Name the parasite shown.
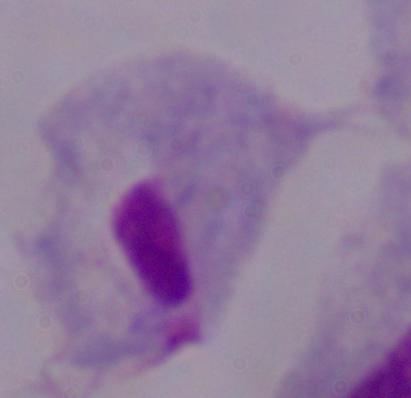

A trichomonad.

{
  "magnification": "1000x",
  "modality": "micrograph"
}